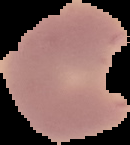

Summary:
  - Result: malaria parasites detected
  - Preparation: thin blood smear
  - Image size: 130×145 pixels
  - Image type: segmented cell region on a black background